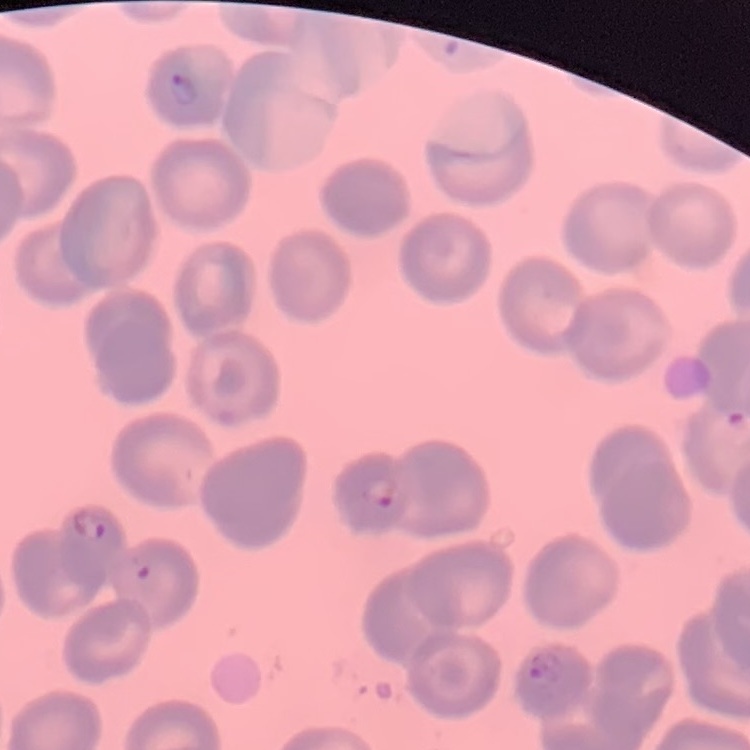

The erythrocytes show no rouleaux formation. Field's or Giemsa stain. Thin blood smear. Square crop of a larger photomicrograph.